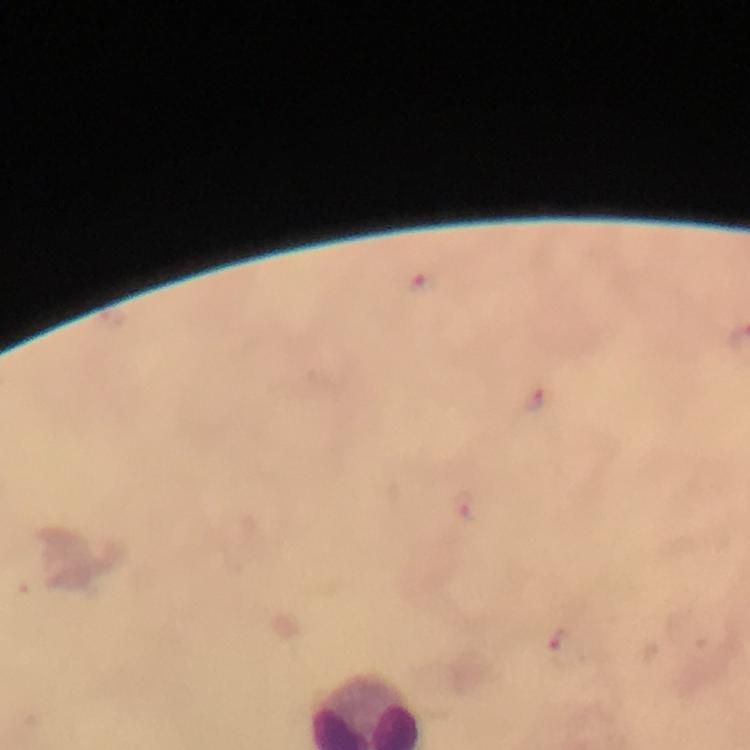
Approximate object centers, in pixels from the top-left corner. Plasmodium parasite locations: (x=421, y=281), (x=537, y=398), (x=560, y=644). A crop from one field of view. Immersion oil was used. Giemsa stain. From a malaria diagnostic workup. Smartphone photograph taken through a microscope. Thick blood smear. Image is 750×750 pixels. 100x magnification.